Assess the morphology of the red blood cells.
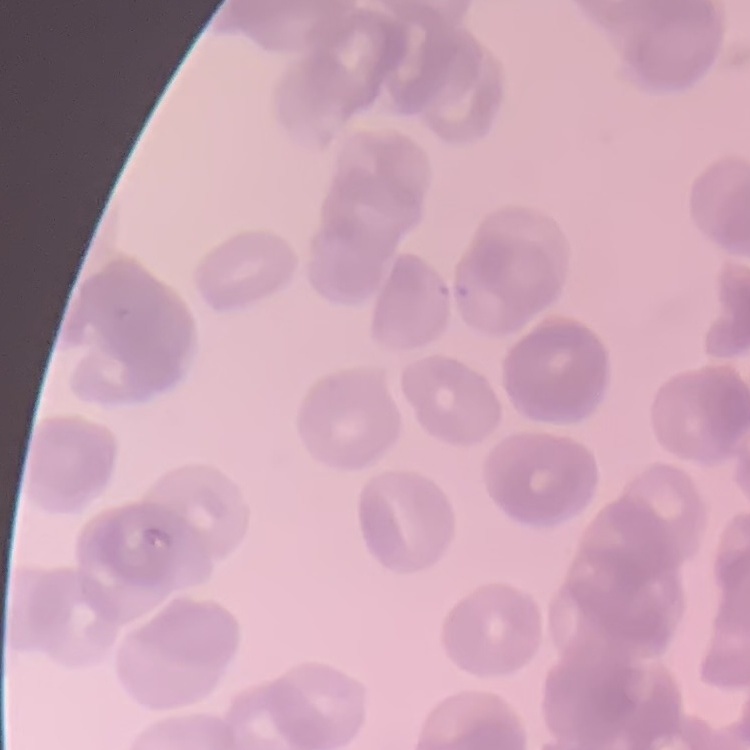

They show rouleaux formation.

Summary:
  - Stain: Field's or Giemsa
  - Image type: one tile cut from a larger photomicrograph
  - Preparation: thin blood smear